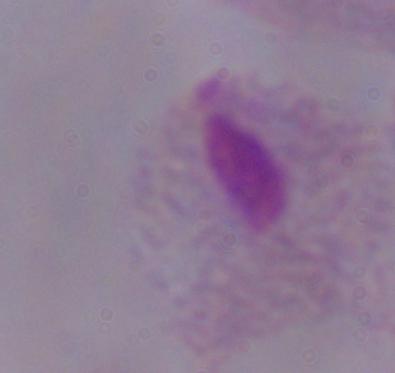
identification = trichomonad
modality = photomicrograph
magnification = 1000x